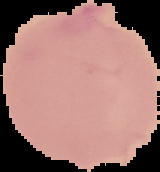

malaria status = uninfected
image type = segmented cell region on a black background
image size = 160×172 pixels
preparation = thin blood smear